Identify the cell.
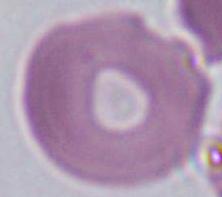

An erythrocyte.

modality = micrograph
magnification = 1000x